Identify the preparation type.
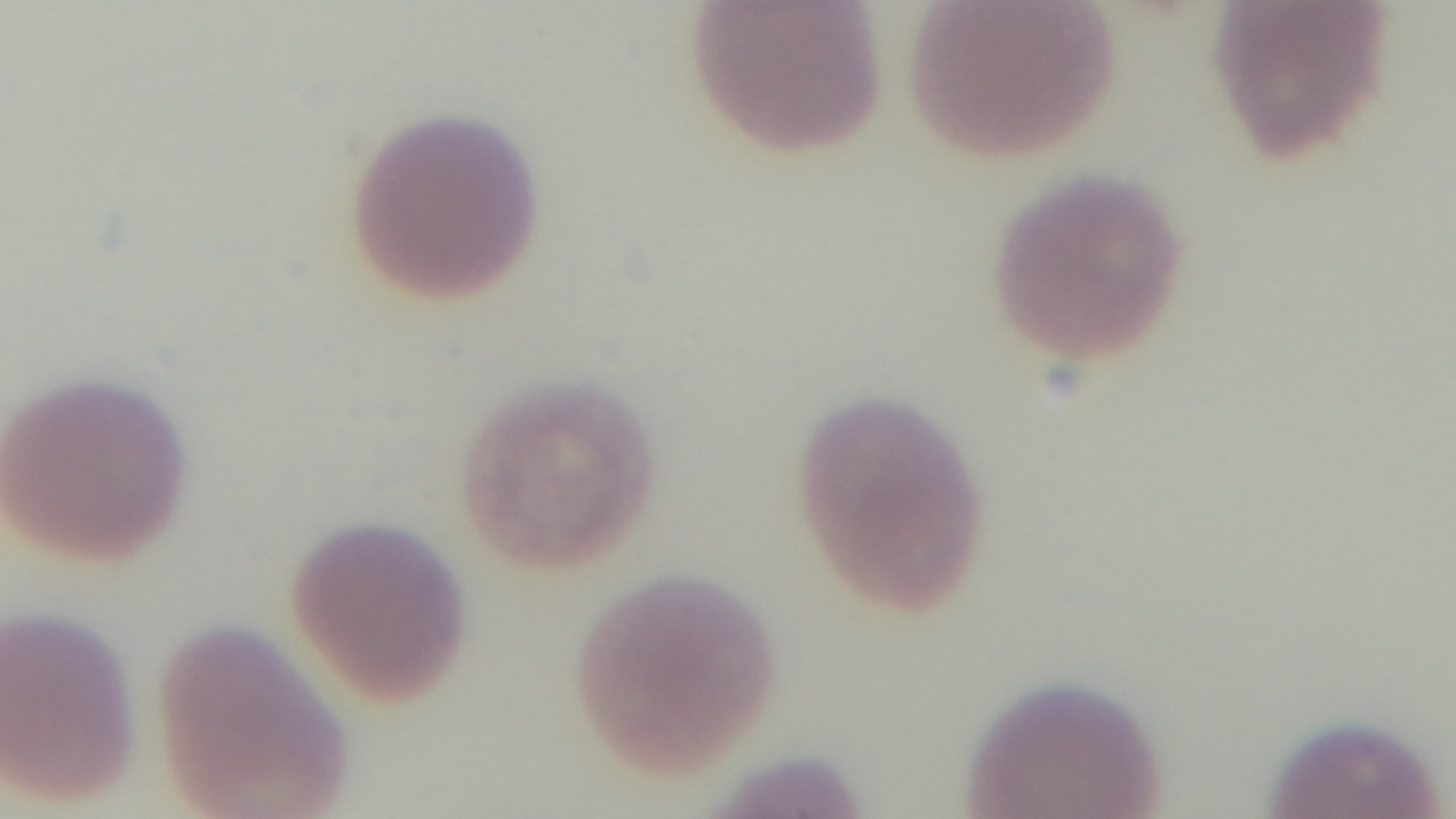
It is a thin blood film.

Summary:
  - Objective: 100x oil immersion
  - Modality: light microscopy
  - Capture: mounted 4K digital camera
  - Malaria status: infected
  - Stain: Giemsa
  - Field of view: one from the slide